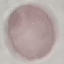

Result: no malaria parasites detected. Thin blood film. Cell patch, automatically extracted from a larger field of view and resized to 64 × 64 pixels. Acquired by smartphone through the microscope eyepiece. Giemsa-stained preparation.